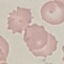
Summary:
  - Malaria status: uninfected
  - Preparation: thin blood smear
  - Image type: cell patch, automatically extracted from a larger field of view and resized to 64 × 64 pixels
  - Stain: Giemsa
  - Capture: smartphone camera at the microscope eyepiece